Classify this cell by malaria status.
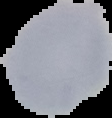
It is uninfected.

Image is 112×118 pixels. Cell region segmented out of the field of view; the surrounding area is masked to black. From a thin blood smear.